Classify this cell by malaria status.
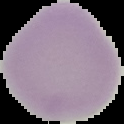

Uninfected.

image type = cell region segmented out of the field of view; surrounding area masked to black
preparation = thin blood film
image size = 124×124 pixels